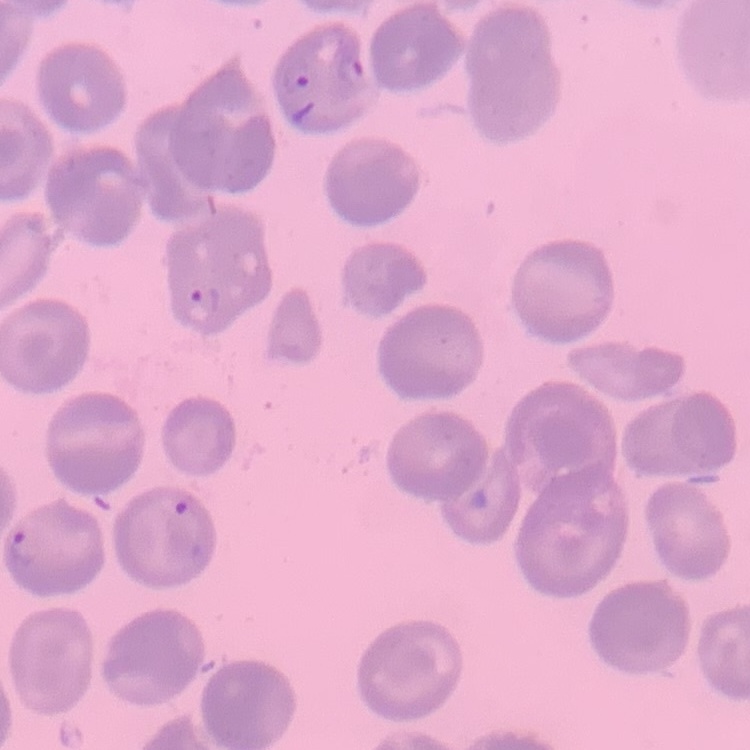

erythrocyte_morphology: no rouleaux formation
stain: Field's or Giemsa
preparation: thin blood film
image_type: one tile cut from a larger photomicrograph